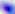

identification: Toxoplasma gondii
magnification: 400x
modality: photomicrograph